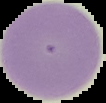
Segmented cell region on a black background. From a thin blood film. Result: negative for Plasmodium parasites. Image is 106×103 pixels.